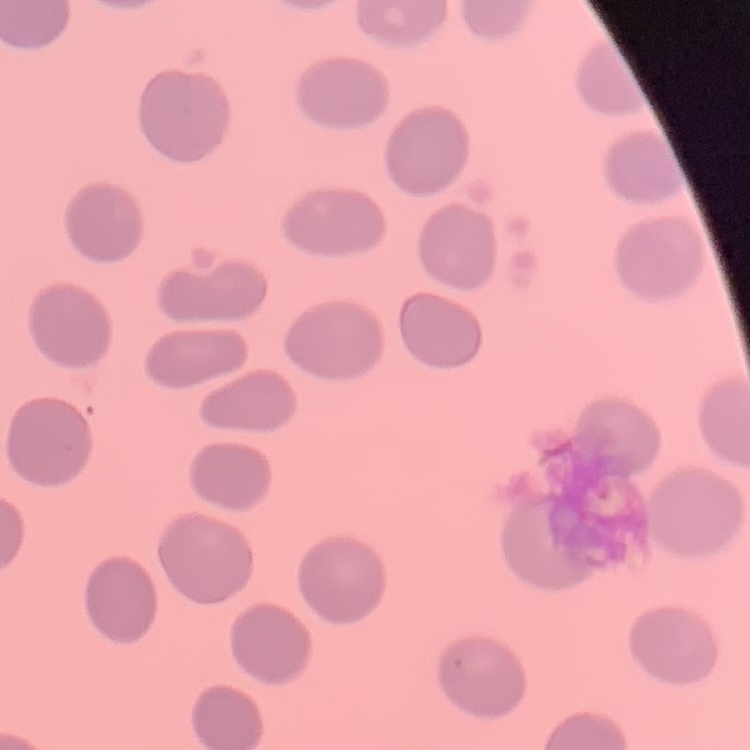
red blood cell morphology = no rouleaux formation
preparation = thin peripheral smear
stain = Field's or Giemsa
image type = one tile cut from a larger photomicrograph